Report the malaria status of this cell.
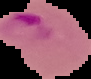
It is parasitized.

Summary:
  - Image type: segmented cell region on a black background
  - Image size: 91×79 pixels
  - Preparation: thin blood film